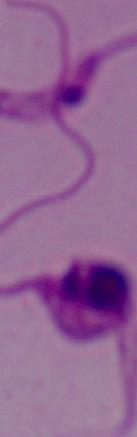

modality = micrograph
magnification = 1000x
identification = Leishmania